Identify the blood parasite species.
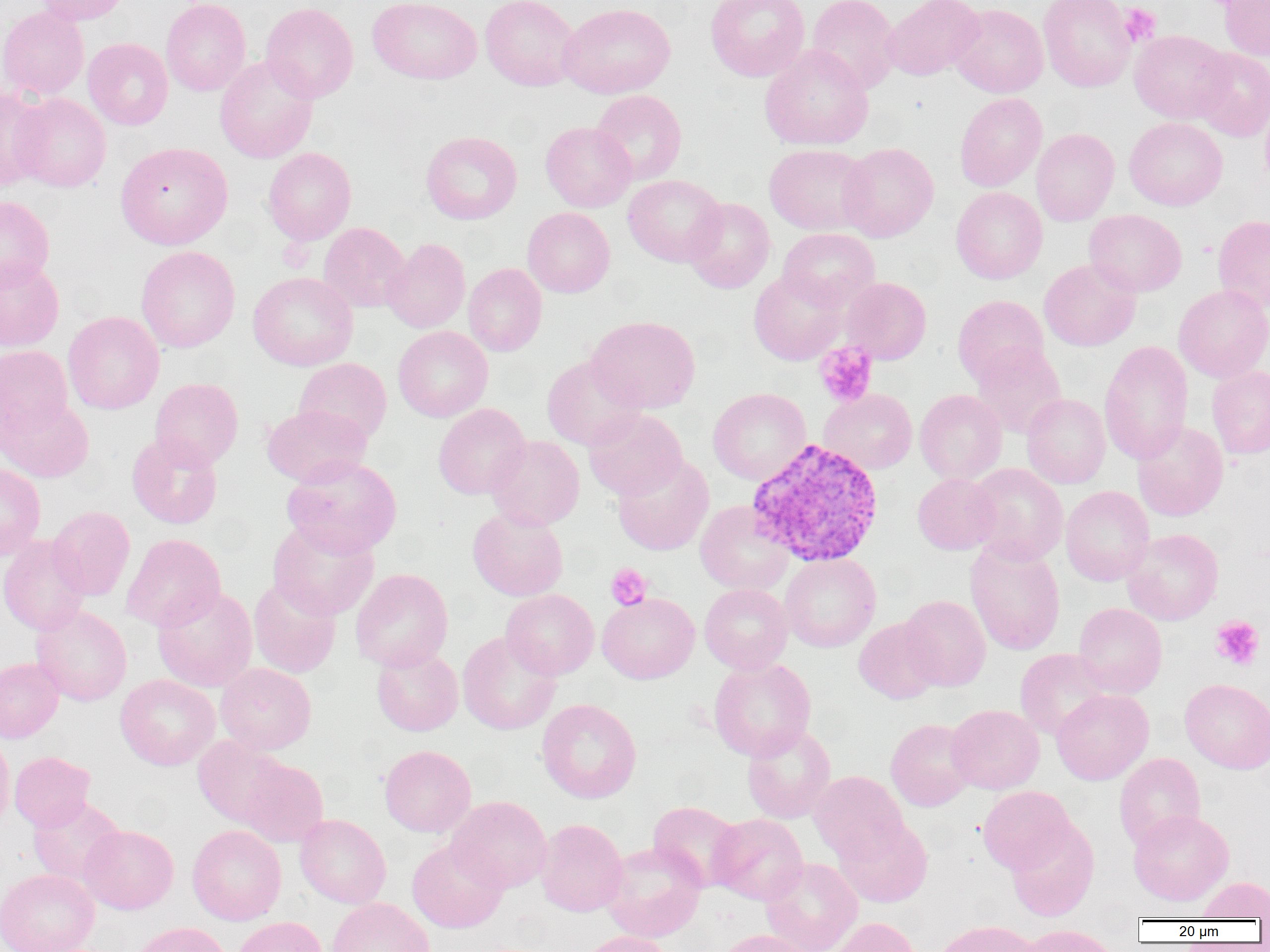

Plasmodium vivax.

Approximate bounding boxes as named x1/y1/x2/y2 corners in pixels. Platelet locations: (x1=1119, y1=3, x2=1161, y2=47), (x1=815, y1=342, x2=877, y2=407), (x1=605, y1=563, x2=652, y2=610), (x1=1211, y1=616, x2=1264, y2=670). Uninfected red blood cell locations: (x1=34, y1=0, x2=130, y2=25), (x1=161, y1=0, x2=251, y2=96), (x1=368, y1=0, x2=482, y2=84), (x1=480, y1=0, x2=580, y2=91), (x1=706, y1=0, x2=810, y2=81), (x1=807, y1=0, x2=900, y2=94), (x1=882, y1=0, x2=984, y2=81), (x1=1039, y1=0, x2=1136, y2=92), (x1=1220, y1=1, x2=1270, y2=60), (x1=260, y1=2, x2=358, y2=103), (x1=559, y1=3, x2=676, y2=99), (x1=949, y1=3, x2=1048, y2=98), (x1=0, y1=7, x2=89, y2=100), (x1=1130, y1=30, x2=1232, y2=123), (x1=83, y1=38, x2=173, y2=130), (x1=760, y1=44, x2=873, y2=150), (x1=1191, y1=47, x2=1270, y2=141), (x1=215, y1=55, x2=318, y2=164), (x1=0, y1=87, x2=50, y2=191), (x1=590, y1=90, x2=687, y2=185), (x1=11, y1=93, x2=111, y2=192), (x1=955, y1=93, x2=1047, y2=191), (x1=1259, y1=99, x2=1270, y2=192), (x1=1124, y1=117, x2=1228, y2=210), (x1=540, y1=121, x2=636, y2=212), (x1=1031, y1=128, x2=1119, y2=226), (x1=421, y1=131, x2=522, y2=224), (x1=115, y1=141, x2=233, y2=250), (x1=838, y1=142, x2=939, y2=242), (x1=764, y1=144, x2=873, y2=235), (x1=262, y1=147, x2=356, y2=245), (x1=623, y1=175, x2=726, y2=266), (x1=951, y1=187, x2=1047, y2=284), (x1=0, y1=196, x2=54, y2=289), (x1=683, y1=198, x2=775, y2=293), (x1=522, y1=207, x2=614, y2=297), (x1=1084, y1=209, x2=1186, y2=297), (x1=1212, y1=214, x2=1270, y2=313), (x1=318, y1=222, x2=410, y2=312), (x1=778, y1=228, x2=880, y2=310), (x1=382, y1=238, x2=471, y2=333), (x1=136, y1=246, x2=240, y2=352), (x1=0, y1=258, x2=64, y2=351), (x1=1039, y1=258, x2=1141, y2=351), (x1=463, y1=263, x2=547, y2=356), (x1=748, y1=270, x2=847, y2=365), (x1=248, y1=271, x2=358, y2=370), (x1=841, y1=277, x2=931, y2=364), (x1=1174, y1=285, x2=1270, y2=382), (x1=952, y1=295, x2=1049, y2=387), (x1=63, y1=311, x2=164, y2=414), (x1=587, y1=315, x2=700, y2=413), (x1=393, y1=326, x2=493, y2=422), (x1=1099, y1=340, x2=1193, y2=465), (x1=972, y1=344, x2=1066, y2=438), (x1=0, y1=345, x2=72, y2=438), (x1=542, y1=355, x2=645, y2=450), (x1=293, y1=357, x2=392, y2=445), (x1=1207, y1=366, x2=1270, y2=460), (x1=150, y1=378, x2=243, y2=470), (x1=708, y1=387, x2=811, y2=484), (x1=819, y1=389, x2=917, y2=474), (x1=915, y1=389, x2=1007, y2=484), (x1=1022, y1=394, x2=1110, y2=488), (x1=1, y1=396, x2=93, y2=483), (x1=433, y1=403, x2=530, y2=500), (x1=262, y1=404, x2=371, y2=488), (x1=583, y1=408, x2=687, y2=500), (x1=1132, y1=421, x2=1228, y2=521), (x1=126, y1=433, x2=223, y2=529), (x1=486, y1=436, x2=584, y2=530), (x1=612, y1=454, x2=713, y2=555), (x1=282, y1=455, x2=401, y2=557), (x1=0, y1=463, x2=45, y2=560), (x1=966, y1=463, x2=1068, y2=565), (x1=913, y1=473, x2=1000, y2=554), (x1=1060, y1=485, x2=1154, y2=586), (x1=695, y1=500, x2=794, y2=595), (x1=48, y1=506, x2=135, y2=601), (x1=467, y1=507, x2=569, y2=601), (x1=267, y1=520, x2=379, y2=620), (x1=1122, y1=528, x2=1223, y2=625), (x1=120, y1=533, x2=225, y2=632), (x1=0, y1=535, x2=90, y2=635), (x1=965, y1=540, x2=1065, y2=656), (x1=780, y1=553, x2=881, y2=652), (x1=350, y1=568, x2=453, y2=671), (x1=248, y1=578, x2=341, y2=678), (x1=699, y1=584, x2=793, y2=674), (x1=153, y1=585, x2=258, y2=692), (x1=501, y1=589, x2=599, y2=680), (x1=597, y1=593, x2=699, y2=683), (x1=899, y1=595, x2=991, y2=691), (x1=1073, y1=603, x2=1167, y2=698), (x1=31, y1=605, x2=132, y2=706), (x1=854, y1=617, x2=942, y2=704), (x1=457, y1=631, x2=561, y2=735), (x1=371, y1=646, x2=463, y2=736), (x1=1015, y1=648, x2=1112, y2=740), (x1=0, y1=658, x2=64, y2=743), (x1=708, y1=658, x2=816, y2=761), (x1=215, y1=663, x2=316, y2=754), (x1=115, y1=675, x2=220, y2=770), (x1=1180, y1=678, x2=1270, y2=773), (x1=1052, y1=689, x2=1153, y2=784), (x1=536, y1=698, x2=641, y2=803), (x1=946, y1=704, x2=1044, y2=794), (x1=885, y1=718, x2=976, y2=811), (x1=741, y1=724, x2=836, y2=823), (x1=0, y1=732, x2=14, y2=832), (x1=193, y1=736, x2=289, y2=828), (x1=379, y1=745, x2=475, y2=837), (x1=9, y1=751, x2=95, y2=831), (x1=1114, y1=753, x2=1205, y2=851), (x1=238, y1=758, x2=329, y2=847), (x1=809, y1=771, x2=909, y2=864), (x1=978, y1=786, x2=1075, y2=874), (x1=447, y1=795, x2=551, y2=893), (x1=27, y1=797, x2=125, y2=887), (x1=648, y1=801, x2=744, y2=891), (x1=1128, y1=809, x2=1234, y2=906), (x1=294, y1=814, x2=391, y2=909), (x1=709, y1=814, x2=808, y2=905), (x1=835, y1=817, x2=933, y2=907), (x1=536, y1=818, x2=628, y2=917), (x1=1006, y1=818, x2=1099, y2=921), (x1=79, y1=824, x2=179, y2=914), (x1=187, y1=825, x2=286, y2=925), (x1=407, y1=839, x2=507, y2=933), (x1=600, y1=842, x2=706, y2=942), (x1=760, y1=858, x2=862, y2=952), (x1=0, y1=869, x2=99, y2=952), (x1=1198, y1=877, x2=1270, y2=920), (x1=327, y1=898, x2=434, y2=952), (x1=232, y1=916, x2=328, y2=952), (x1=827, y1=917, x2=921, y2=952), (x1=931, y1=920, x2=1039, y2=952), (x1=130, y1=921, x2=232, y2=952), (x1=1016, y1=925, x2=1121, y2=952), (x1=714, y1=929, x2=817, y2=952), (x1=576, y1=930, x2=675, y2=952). Plasmodium vivax-infected red blood cell locations: (x1=747, y1=438, x2=883, y2=567). 1000x magnification. Image is 1270×952 pixels. Light microscopy. Thin blood film. One field of a larger specimen.